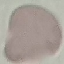

Summary:
  - Result: no malaria parasites seen
  - Capture: smartphone through the microscope eyepiece
  - Stain: Giemsa
  - Image type: automatically extracted cell patch, resized to 64 × 64 pixels
  - Preparation: thin blood film